Draw a bounding box around every leukocyte (white blood cell).
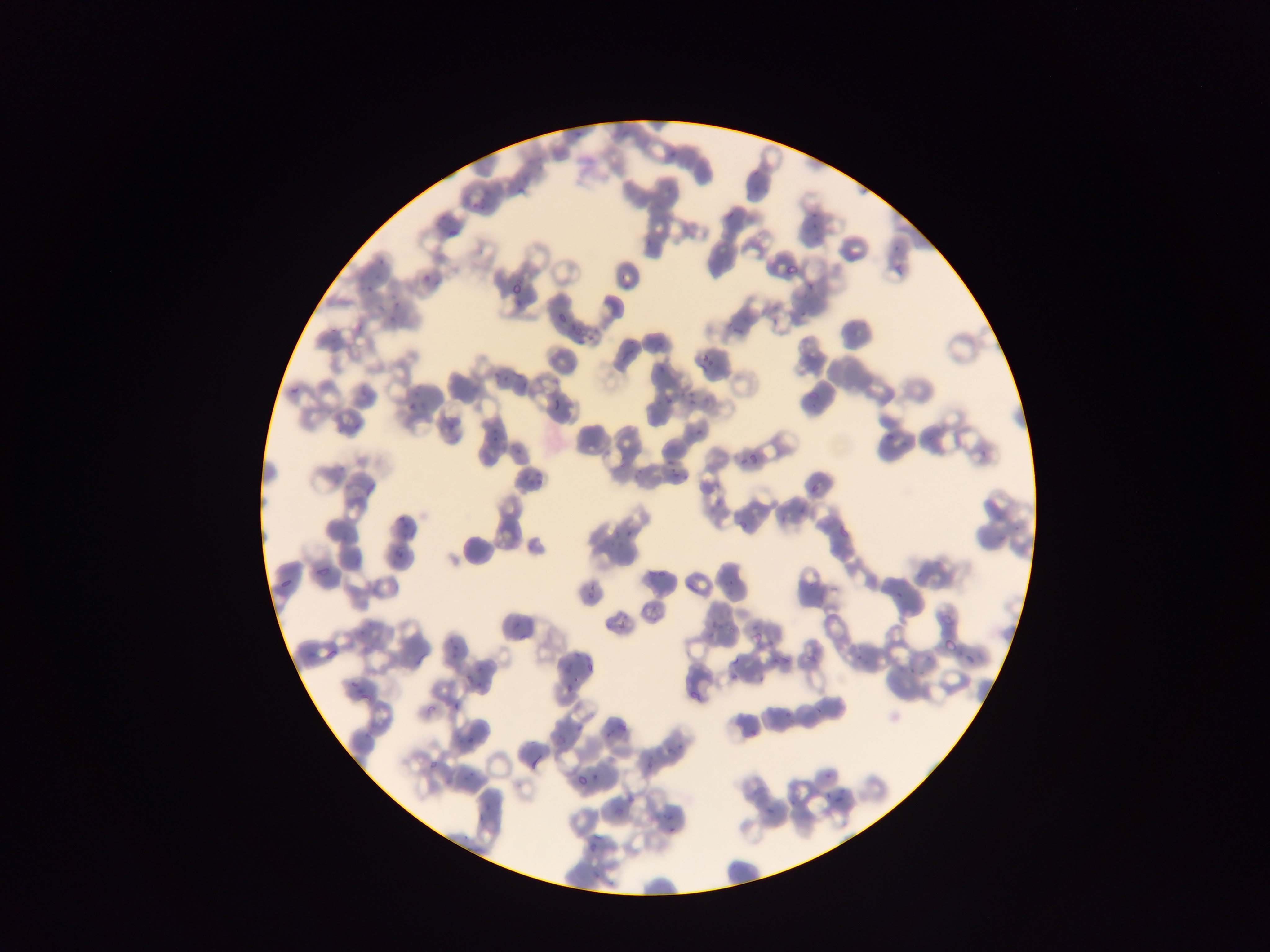
No leukocytes observed.

capture: mobile-phone photograph through a microscope
preparation: thin blood film
image_size: 1270×952 pixels
country: Ghana
plasmodium_parasite_locations: 'approximate bounding boxes as left top right bottom in pixels: 567 132 579 143; 514 181 528 197; 465 193 492 215; 431 207 448 223; 809 211 822 235; 445 226 457 241; 374 257 396 278; 782 258 804 275; 616 263 647 285; 362 273 374 297; 418 273 430 286; 508 278 520 300; 511 299 521 308; 389 305 399 324; 798 307 810 316; 554 309 566 326; 358 318 373 337; 768 321 780 331; 568 322 574 336; 582 330 595 344; 652 330 666 350; 619 349 629 363; 699 352 714 370; 654 364 667 375; 489 366 505 385; 517 372 530 391; 807 379 831 403; 404 381 430 416; 284 382 301 404; 688 389 698 409; 663 392 673 409; 552 396 561 410; 434 410 461 433; 349 415 361 449; 688 419 715 438; 486 423 505 448; 513 445 527 462; 734 449 758 473; 633 458 647 485; 667 469 681 484; 528 472 549 486; 362 474 384 497; 807 477 833 499; 698 478 719 502; 703 504 712 516; 799 508 811 519; 833 509 865 541; 396 515 408 532; 611 516 634 536; 737 519 754 533; 520 541 535 555; 389 548 403 562; 648 556 670 583; 313 559 331 581; 719 574 738 594; 274 578 290 592; 892 578 909 599; 582 581 596 603; 644 599 667 617; 608 613 628 632; 703 618 721 642; 506 622 528 642; 749 627 767 647; 354 629 366 642; 938 629 951 663; 853 643 877 667; 451 645 455 656; 319 646 336 666; 805 647 823 664; 767 648 786 680; 561 653 574 672; 305 655 312 664; 410 655 420 666; 579 655 600 679; 721 655 741 682; 966 655 979 674; 907 663 914 674; 348 668 365 687; 463 671 471 680; 475 672 486 699; 563 686 572 703; 354 688 369 706; 452 701 461 713; 422 705 432 716; 778 705 790 724; 742 717 756 741; 464 719 492 743; 551 719 588 746; 604 725 620 738; 363 729 369 740; 636 749 664 778; 528 753 541 778; 421 763 435 774; 580 764 611 796; 461 771 475 782; 444 776 459 793; 823 788 838 812; 477 797 491 820; 760 803 775 822; 657 804 681 836; 583 829 607 865; 587 874 603 885'
field_of_view: single